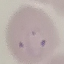
Summary:
  - Malaria status: parasitized
  - Capture: smartphone camera at the microscope eyepiece
  - Stain: Giemsa
  - Image type: automatically extracted cell patch, resized to 64 × 64 pixels
  - Preparation: thin blood smear